Name the cell type shown.
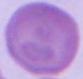

This is an erythrocyte.

Micrograph. Captured at 1000x magnification.